Name the parasite shown.
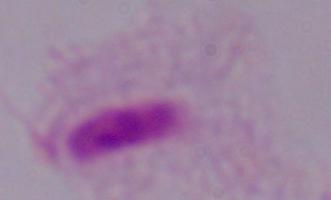

A trichomonad.

magnification = 1000x
modality = photomicrograph